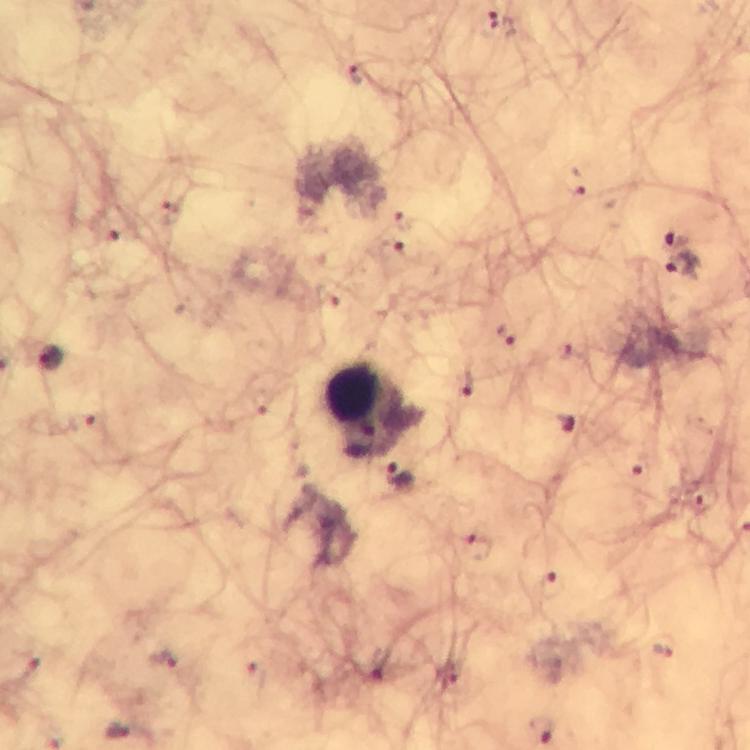

Approximate centers as [x, y] in pixels.
Summary:
  - Plasmodium parasite locations: [502, 26], [355, 70], [576, 183], [403, 218], [116, 232], [679, 236], [407, 249], [682, 264], [507, 336], [51, 357], [467, 383], [83, 422], [566, 423], [638, 468], [397, 476], [701, 497], [477, 547], [551, 585], [664, 649], [161, 657], [23, 663], [366, 669], [256, 678], [120, 731]
  - Leukocyte locations: [374, 409]
  - Context: from a malaria diagnostic workup
  - Magnification: 100x
  - Capture: smartphone camera through the microscope
  - Preparation: thick smear
  - Image size: 750×750 pixels
  - Immersion oil: used
  - Cropped from: a single field of view
  - Stain: Giemsa